Name the cell type shown.
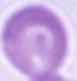

This is an erythrocyte.

Captured at 1000x magnification. Micrograph.